Classify this cell by malaria status.
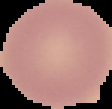
Uninfected.

Summary:
  - Image type: segmented cell region on a black background
  - Image size: 112×109 pixels
  - Preparation: thin blood smear